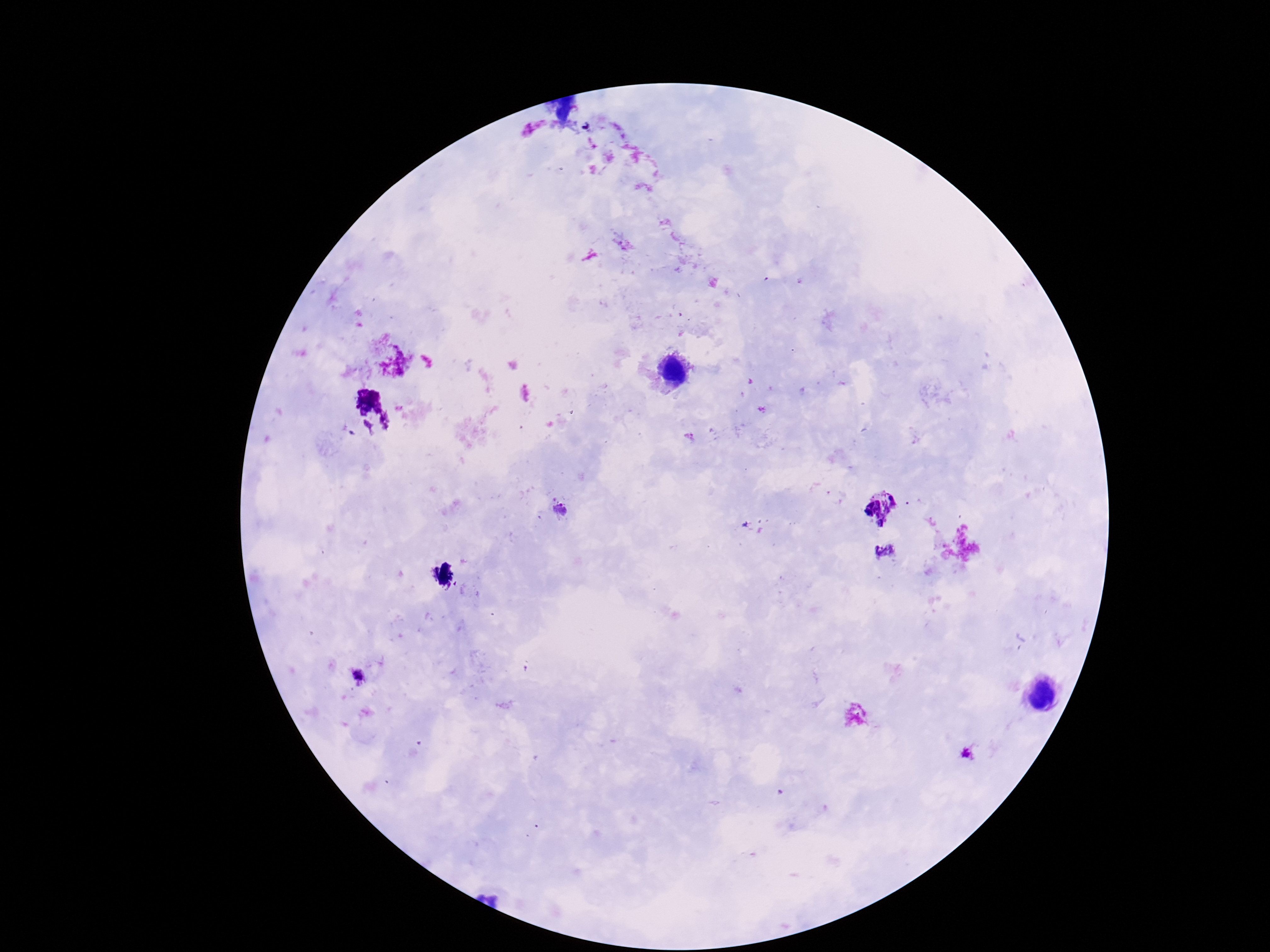
Approximate object centers, in pixels from the top-left corner.
Summary:
  - Plasmodium parasite locations: (x=560, y=510), (x=358, y=676), (x=969, y=757)
  - Patient malaria status: positive
  - Preparation: thick blood film
  - Stain: Giemsa
  - Capture: smartphone camera through the microscope eyepiece
  - Field of view: one from this slide
  - Magnification: 100x
  - Image size: 1270×952 pixels